Evaluate for malaria.
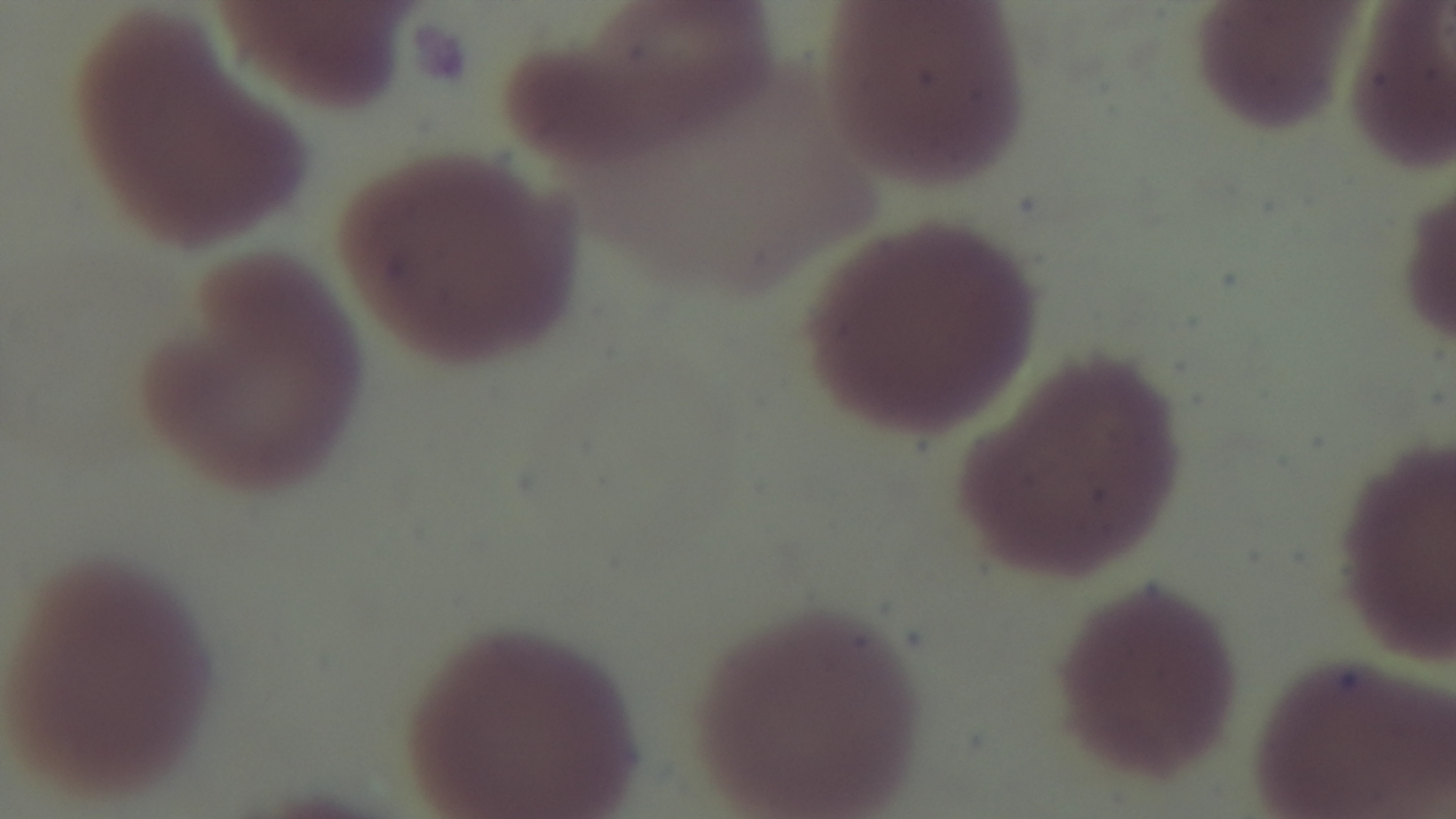
It is uninfected.

Summary:
  - Capture: mounted 4K digital camera
  - Field of view: one from the slide
  - Objective: 100x oil immersion
  - Modality: light microscopy
  - Stain: Giemsa
  - Preparation: thin smear